Locate every blood parasite and identify its species.
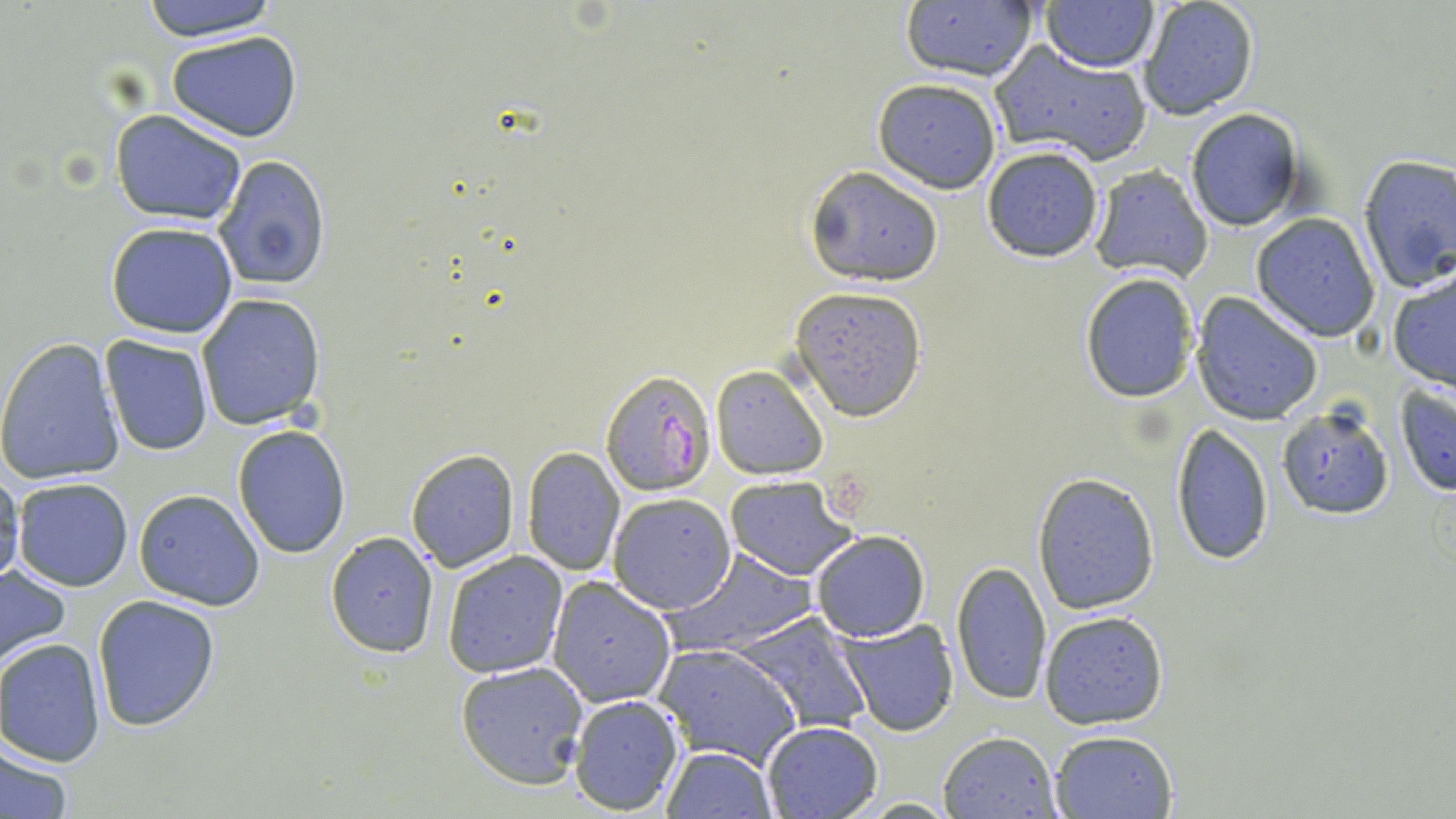

Approximate bounding boxes as (x1, y1, x2, y2) in pixels.
Plasmodium falciparum-infected red blood cells: (600, 369, 717, 493).
No Plasmodium ovale, Plasmodium malariae, Plasmodium vivax, Babesia divergens, or Trypanosoma brucei observed.

Summary:
  - Uninfected red blood cell locations: (137, 0, 281, 43), (900, 1, 1042, 85), (1137, 1, 1261, 121), (1041, 2, 1159, 72), (167, 31, 302, 141), (992, 43, 1153, 166), (872, 78, 1001, 192), (1184, 107, 1307, 232), (110, 110, 248, 226), (981, 145, 1105, 264), (1356, 154, 1456, 293), (213, 155, 332, 291), (803, 164, 946, 285), (1087, 165, 1214, 282), (1251, 212, 1382, 343), (105, 222, 239, 337), (1388, 271, 1456, 390), (1079, 273, 1197, 403), (790, 285, 929, 422), (196, 294, 327, 431), (1192, 294, 1324, 424), (100, 336, 213, 457), (0, 338, 125, 486), (710, 364, 828, 479), (1393, 380, 1456, 496), (1276, 406, 1394, 518), (232, 424, 349, 557), (1172, 424, 1275, 564), (520, 445, 625, 575), (404, 448, 519, 571), (0, 467, 24, 591), (1031, 472, 1162, 615), (726, 476, 858, 581), (12, 477, 134, 591), (133, 489, 266, 610), (607, 492, 737, 612), (326, 530, 440, 658), (810, 532, 928, 642), (441, 550, 568, 678), (669, 550, 815, 655), (950, 560, 1052, 706), (0, 563, 73, 672), (547, 576, 677, 708), (92, 594, 222, 730), (1038, 609, 1172, 731), (730, 612, 873, 735), (838, 619, 960, 737), (0, 637, 106, 765), (655, 642, 802, 767), (456, 662, 589, 787), (568, 693, 685, 813), (760, 720, 884, 817), (1049, 729, 1179, 817), (937, 730, 1062, 817), (0, 744, 74, 819), (660, 746, 776, 818)
  - Slide-level diagnosis: Plasmodium falciparum
  - Modality: optical microscopy
  - Image size: 1456×819 pixels
  - Field of view: single
  - Preparation: thin blood smear
  - Stain: May-Grünwald-Giemsa
  - Magnification: 1000x